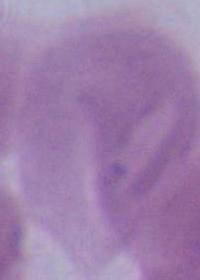

Summary:
  - Identification: red blood cell
  - Magnification: 1000x
  - Modality: photomicrograph